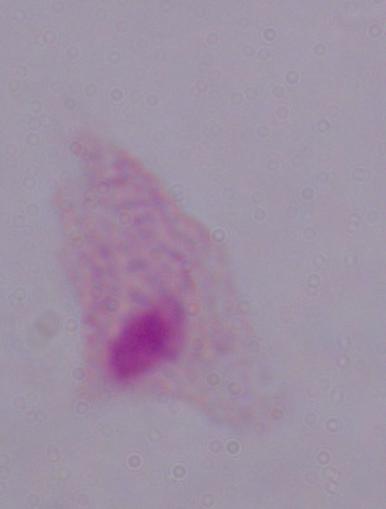

modality = photomicrograph
magnification = 1000x
identification = trichomonad